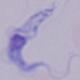
Photomicrograph. Captured at 1000x magnification. A trypanosome is seen.